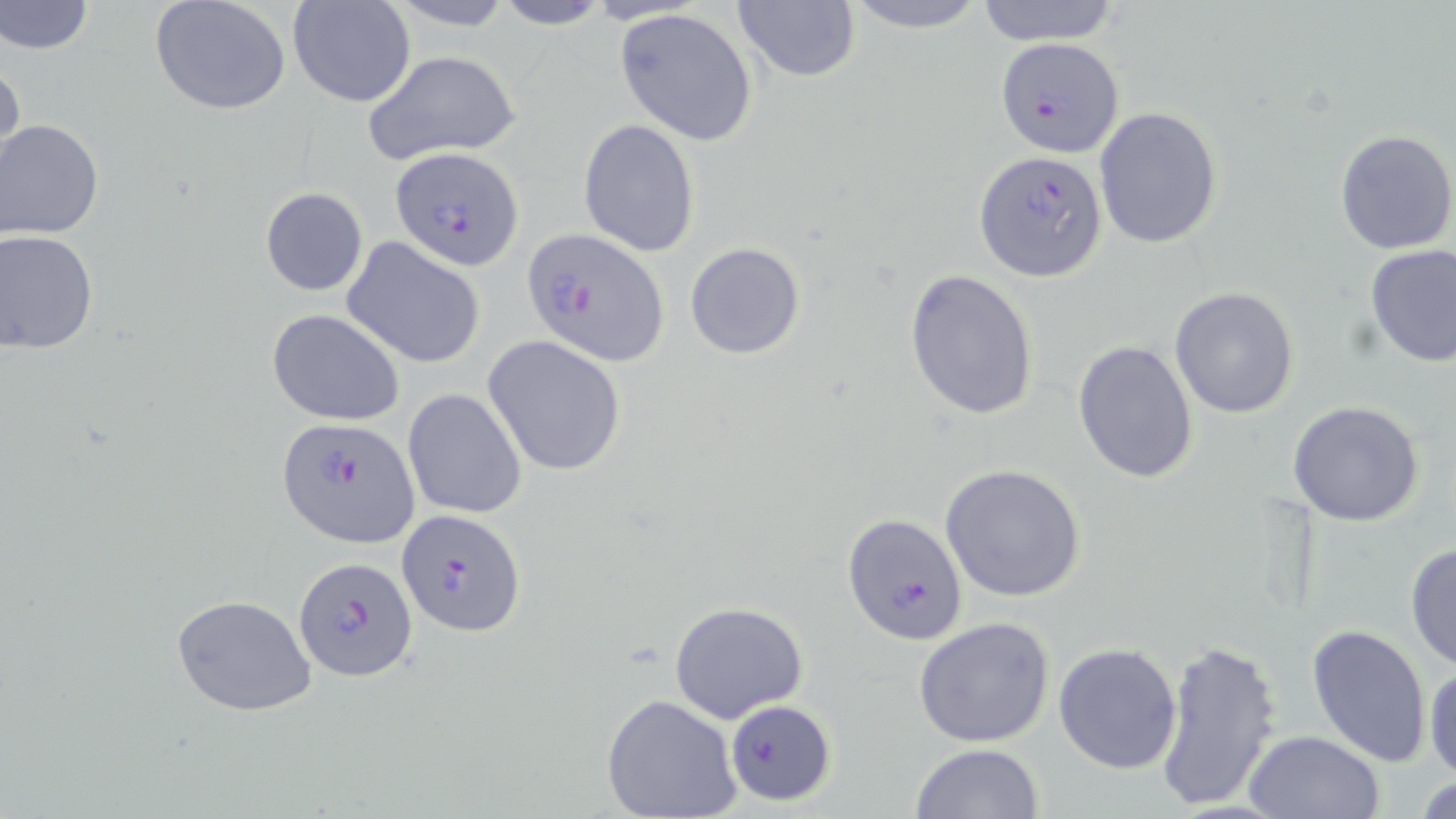
slide_level_diagnosis: Plasmodium falciparum
image_size: 1456×819 pixels
field_of_view: one of a larger specimen
modality: light microscopy
plasmodium_falciparum_infected_red_blood_cell_locations: 'approximate bounding boxes as named x1/y1/x2/y2 corners in pixels: (x1=996, y1=35, x2=1123, y2=155), (x1=392, y1=146, x2=522, y2=270), (x1=974, y1=150, x2=1106, y2=282), (x1=522, y1=227, x2=668, y2=366), (x1=277, y1=418, x2=421, y2=548), (x1=396, y1=508, x2=524, y2=638), (x1=843, y1=512, x2=966, y2=645), (x1=296, y1=556, x2=416, y2=681), (x1=726, y1=700, x2=836, y2=805)'
uninfected_red_blood_cell_locations: 'approximate bounding boxes as named x1/y1/x2/y2 corners in pixels: (x1=1, y1=0, x2=95, y2=55), (x1=148, y1=0, x2=291, y2=116), (x1=288, y1=0, x2=417, y2=106), (x1=489, y1=0, x2=616, y2=30), (x1=838, y1=0, x2=994, y2=34), (x1=385, y1=1, x2=519, y2=32), (x1=733, y1=1, x2=861, y2=85), (x1=970, y1=1, x2=1125, y2=45), (x1=613, y1=7, x2=760, y2=146), (x1=362, y1=49, x2=522, y2=164), (x1=0, y1=52, x2=26, y2=179), (x1=1094, y1=106, x2=1223, y2=251), (x1=578, y1=119, x2=701, y2=258), (x1=0, y1=120, x2=107, y2=240), (x1=1333, y1=128, x2=1456, y2=255), (x1=259, y1=186, x2=367, y2=296), (x1=1, y1=230, x2=100, y2=354), (x1=342, y1=237, x2=485, y2=368), (x1=685, y1=242, x2=805, y2=358), (x1=1363, y1=245, x2=1456, y2=368), (x1=904, y1=271, x2=1041, y2=420), (x1=1169, y1=286, x2=1298, y2=417), (x1=266, y1=308, x2=406, y2=426), (x1=481, y1=334, x2=628, y2=476), (x1=1073, y1=340, x2=1199, y2=486), (x1=401, y1=389, x2=527, y2=519), (x1=1286, y1=401, x2=1426, y2=526), (x1=939, y1=463, x2=1086, y2=601), (x1=1405, y1=541, x2=1456, y2=670), (x1=171, y1=595, x2=317, y2=716), (x1=668, y1=601, x2=808, y2=723), (x1=913, y1=617, x2=1056, y2=749), (x1=1308, y1=624, x2=1433, y2=766), (x1=1153, y1=638, x2=1282, y2=816), (x1=1053, y1=641, x2=1183, y2=773), (x1=1425, y1=662, x2=1456, y2=783), (x1=602, y1=694, x2=744, y2=819), (x1=1243, y1=729, x2=1385, y2=819), (x1=910, y1=743, x2=1045, y2=819)'
magnification: 1000x
preparation: thin blood smear
stain: May-Grünwald-Giemsa